Name the parasite shown.
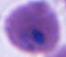

Plasmodium.

magnification: 400x or 1000x
modality: photomicrograph